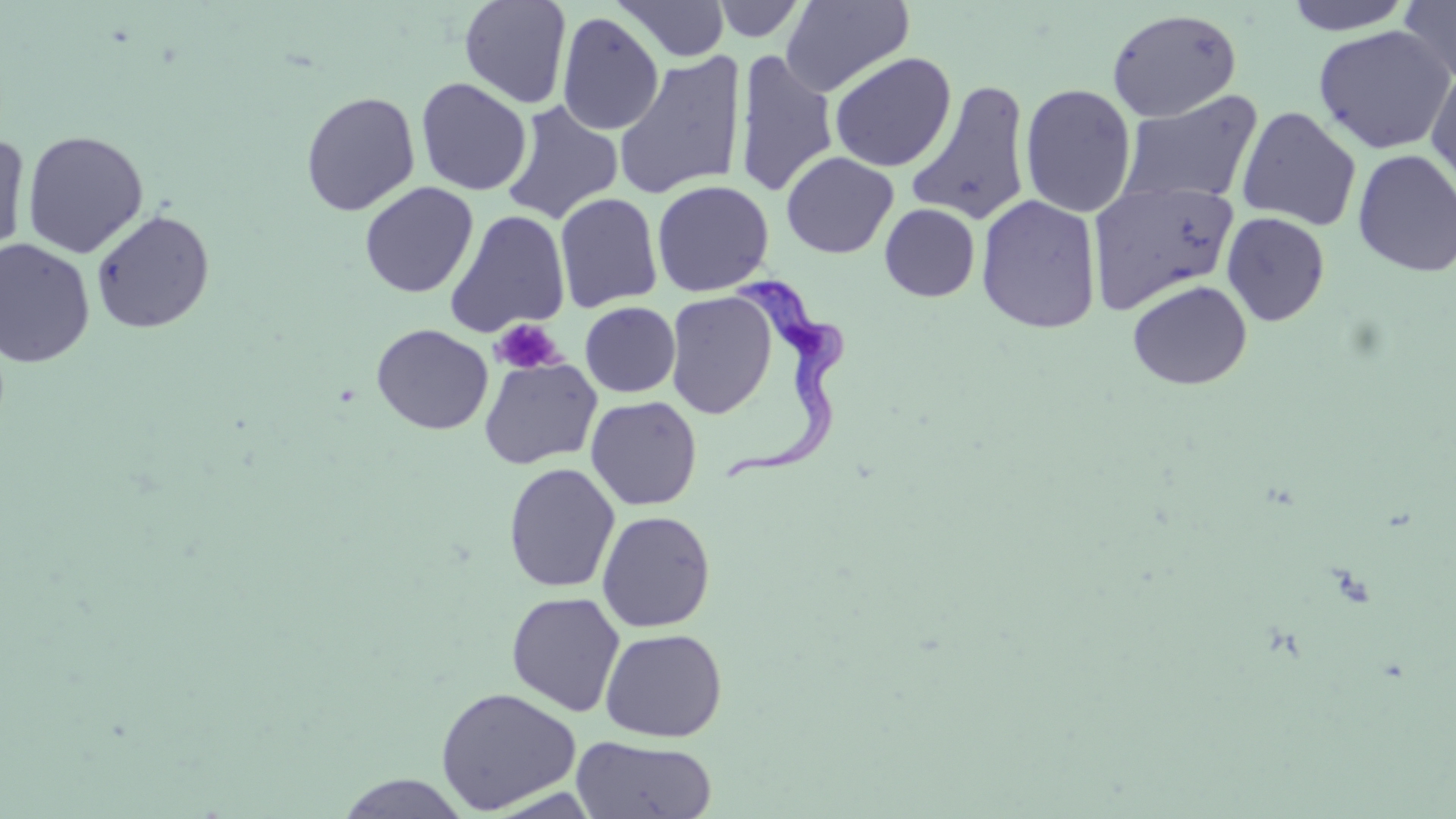

slide-level diagnosis = Trypanosoma brucei
uninfected red blood cell locations = approximate bounding boxes as (x1, y1, x2, y2) in pixels: (459, 0, 572, 108), (711, 0, 806, 42), (780, 0, 914, 96), (1283, 0, 1415, 34), (1399, 0, 1456, 84), (615, 1, 730, 62), (1107, 8, 1242, 122), (557, 11, 664, 135), (1313, 25, 1455, 154), (734, 49, 838, 197), (613, 51, 747, 201), (829, 52, 957, 172), (1426, 64, 1456, 195), (416, 77, 532, 196), (906, 80, 1033, 227), (1019, 83, 1137, 217), (1118, 90, 1263, 207), (300, 91, 420, 216), (500, 100, 624, 224), (1237, 106, 1361, 231), (22, 130, 149, 258), (0, 133, 31, 261), (1352, 149, 1456, 277), (781, 151, 899, 259), (651, 179, 774, 296), (1088, 180, 1239, 313), (359, 181, 478, 298), (554, 192, 662, 313), (975, 194, 1102, 334), (880, 203, 980, 302), (91, 209, 216, 334), (445, 210, 570, 338), (1222, 211, 1330, 326), (0, 239, 95, 368), (1127, 280, 1252, 390), (665, 291, 778, 419), (580, 301, 680, 397), (371, 324, 493, 434), (479, 356, 601, 469), (585, 395, 702, 510), (503, 463, 620, 593), (596, 510, 716, 633), (506, 591, 625, 716), (599, 627, 727, 742), (434, 686, 582, 814), (571, 736, 717, 818), (335, 773, 472, 818)
stain = May-Grünwald-Giemsa
platelet locations = approximate bounding boxes as (x1, y1, x2, y2) in pixels: (491, 318, 564, 374)
Trypanosoma brucei locations = approximate bounding boxes as (x1, y1, x2, y2) in pixels: (710, 269, 852, 483)
field of view = single
image size = 1456×819 pixels
preparation = thin blood film
magnification = 1000x
modality = optical microscopy